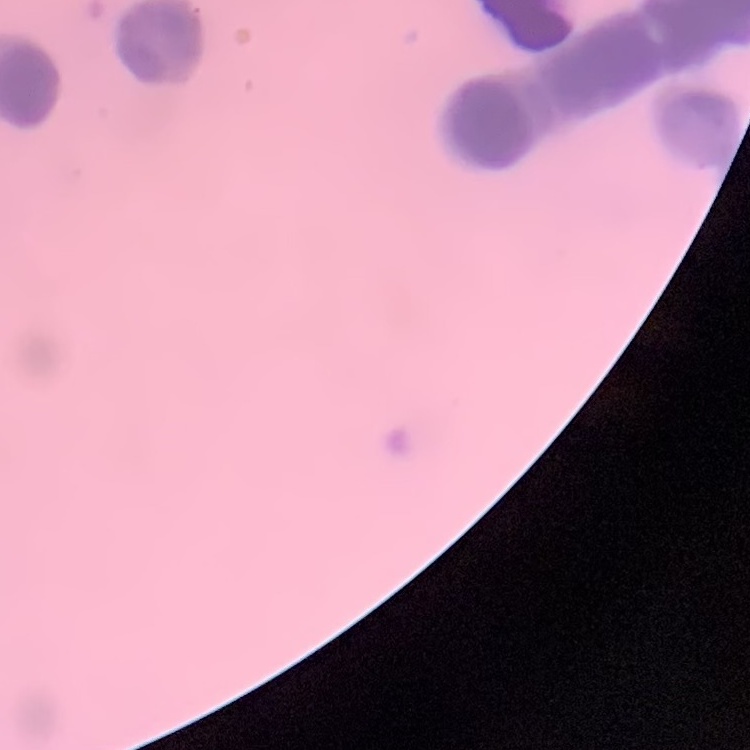
red blood cell morphology = rouleaux formation
preparation = thin peripheral smear
image type = square crop of a larger photomicrograph
stain = Field's or Giemsa